Name the parasite shown.
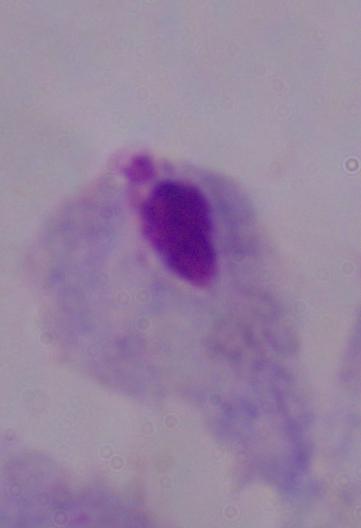
A trichomonad.

Photomicrograph. Captured at 1000x magnification.